Outline each blood parasite and name the species.
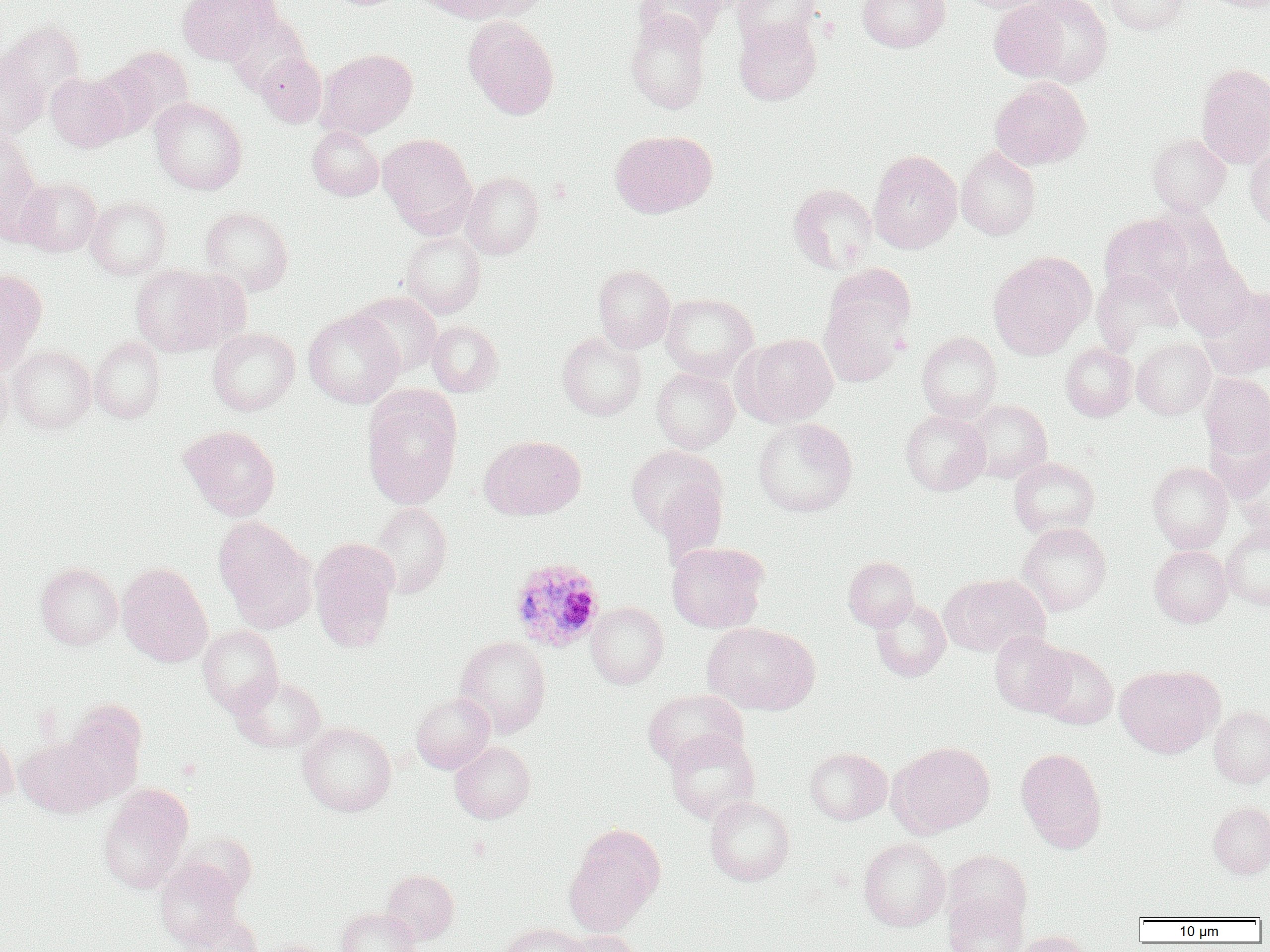

Approximate bounding boxes as (x1, y1, x2, y2) in pixels.
Plasmodium ovale-infected red blood cells: (509, 558, 605, 652).
No Plasmodium falciparum, Plasmodium malariae, Plasmodium vivax, Babesia divergens, or Trypanosoma brucei observed.

Uninfected red blood cell locations: (177, 0, 276, 64), (424, 0, 537, 23), (635, 0, 727, 46), (733, 0, 822, 51), (857, 0, 949, 52), (958, 0, 1055, 13), (1105, 0, 1189, 35), (1202, 0, 1270, 11), (989, 1, 1069, 82), (1017, 1, 1114, 88), (223, 9, 310, 92), (626, 10, 711, 113), (463, 16, 559, 119), (734, 18, 821, 105), (1, 21, 87, 112), (99, 45, 194, 135), (317, 49, 418, 139), (0, 51, 47, 140), (255, 53, 326, 127), (1195, 63, 1270, 169), (45, 72, 129, 151), (990, 78, 1091, 170), (149, 97, 247, 194), (307, 126, 383, 201), (610, 130, 713, 218), (0, 132, 42, 235), (1147, 132, 1231, 215), (378, 134, 477, 237), (1245, 145, 1270, 228), (956, 146, 1040, 240), (868, 149, 962, 254), (461, 171, 544, 259), (17, 176, 102, 256), (788, 183, 878, 273), (85, 197, 170, 279), (1147, 204, 1233, 290), (201, 206, 294, 295), (1100, 214, 1192, 298), (401, 230, 485, 318), (988, 251, 1095, 358), (1171, 254, 1254, 339), (130, 264, 230, 356), (593, 264, 675, 352), (825, 264, 916, 345), (0, 268, 47, 363), (1092, 269, 1182, 352), (1198, 286, 1270, 378), (351, 292, 442, 376), (659, 293, 757, 381), (819, 296, 908, 387), (303, 309, 404, 408), (426, 320, 502, 396), (207, 328, 299, 415), (557, 330, 646, 420), (916, 331, 1002, 421), (737, 333, 838, 426), (88, 336, 166, 423), (1132, 337, 1216, 420), (1061, 342, 1137, 421), (8, 344, 95, 433), (0, 363, 13, 442), (651, 367, 739, 453), (1200, 373, 1270, 457), (361, 386, 463, 509), (965, 400, 1051, 482), (900, 409, 991, 495), (753, 418, 858, 517), (180, 425, 280, 520), (480, 435, 585, 519), (626, 444, 727, 546), (1229, 445, 1270, 537), (1009, 457, 1099, 536), (1148, 461, 1233, 552), (369, 502, 452, 598), (213, 517, 317, 630), (1018, 522, 1111, 615), (1221, 523, 1270, 609), (309, 538, 399, 652), (667, 542, 768, 633), (1150, 545, 1232, 627), (843, 556, 919, 631), (35, 561, 123, 649), (117, 563, 213, 667), (940, 572, 1050, 657), (870, 597, 950, 682), (586, 602, 668, 688), (702, 621, 818, 715), (198, 625, 283, 715), (989, 631, 1074, 717), (455, 636, 551, 736), (1032, 645, 1118, 729), (1115, 665, 1219, 757), (230, 674, 326, 752), (643, 689, 748, 772), (410, 692, 495, 773), (59, 701, 146, 805), (1209, 706, 1270, 787), (297, 722, 396, 816), (665, 729, 760, 824), (0, 730, 18, 803), (15, 736, 107, 817), (450, 741, 535, 823), (888, 741, 995, 837), (805, 747, 891, 825), (1016, 747, 1107, 852), (98, 785, 193, 893), (705, 796, 795, 885), (1208, 801, 1270, 878), (564, 823, 666, 934), (858, 837, 950, 931), (943, 850, 1031, 930), (155, 859, 244, 950), (382, 869, 459, 945), (943, 893, 1026, 952), (336, 907, 421, 952), (182, 912, 262, 952), (500, 923, 588, 952), (558, 929, 646, 952), (1013, 930, 1093, 952), (257, 938, 332, 952). Slide-level diagnosis: Plasmodium ovale. 1000x magnification. Light microscopy. Image is 1270×952 pixels. Single field of view. Thin blood film.